Identify the parasite.
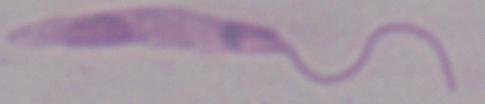

Leishmania.

Micrograph. Captured at 1000x magnification.